Give the preparation type.
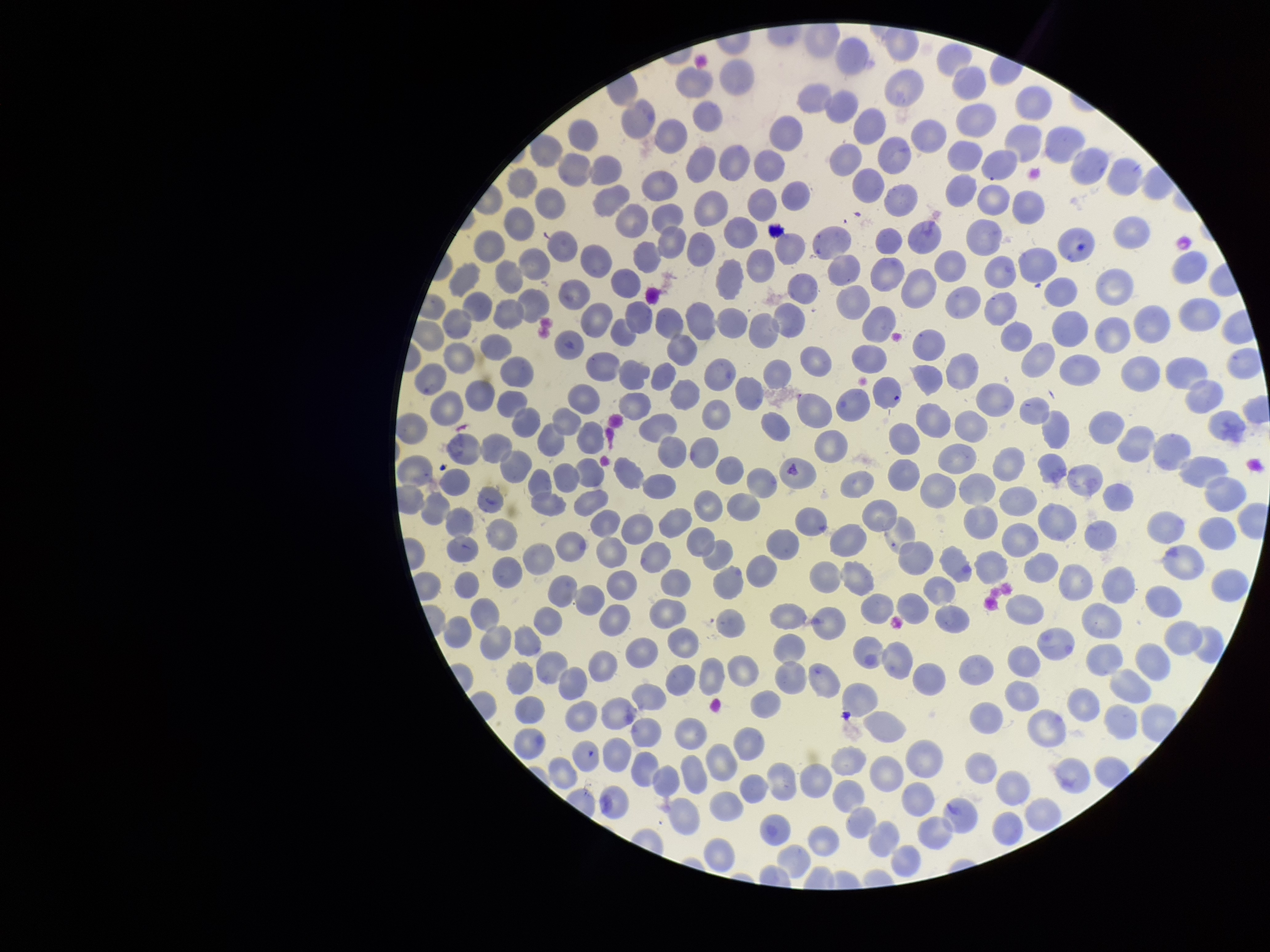

It is a thin blood smear.

Photographed through the microscope eyepiece with a smartphone camera. Parasitized red blood cell count: 0. Single field of view. Red blood cell count: 317. Parasitized red blood cells: none seen. Patient malaria status: negative. Image is 1270×952 pixels. Stained with Giemsa.